Report the malaria status.
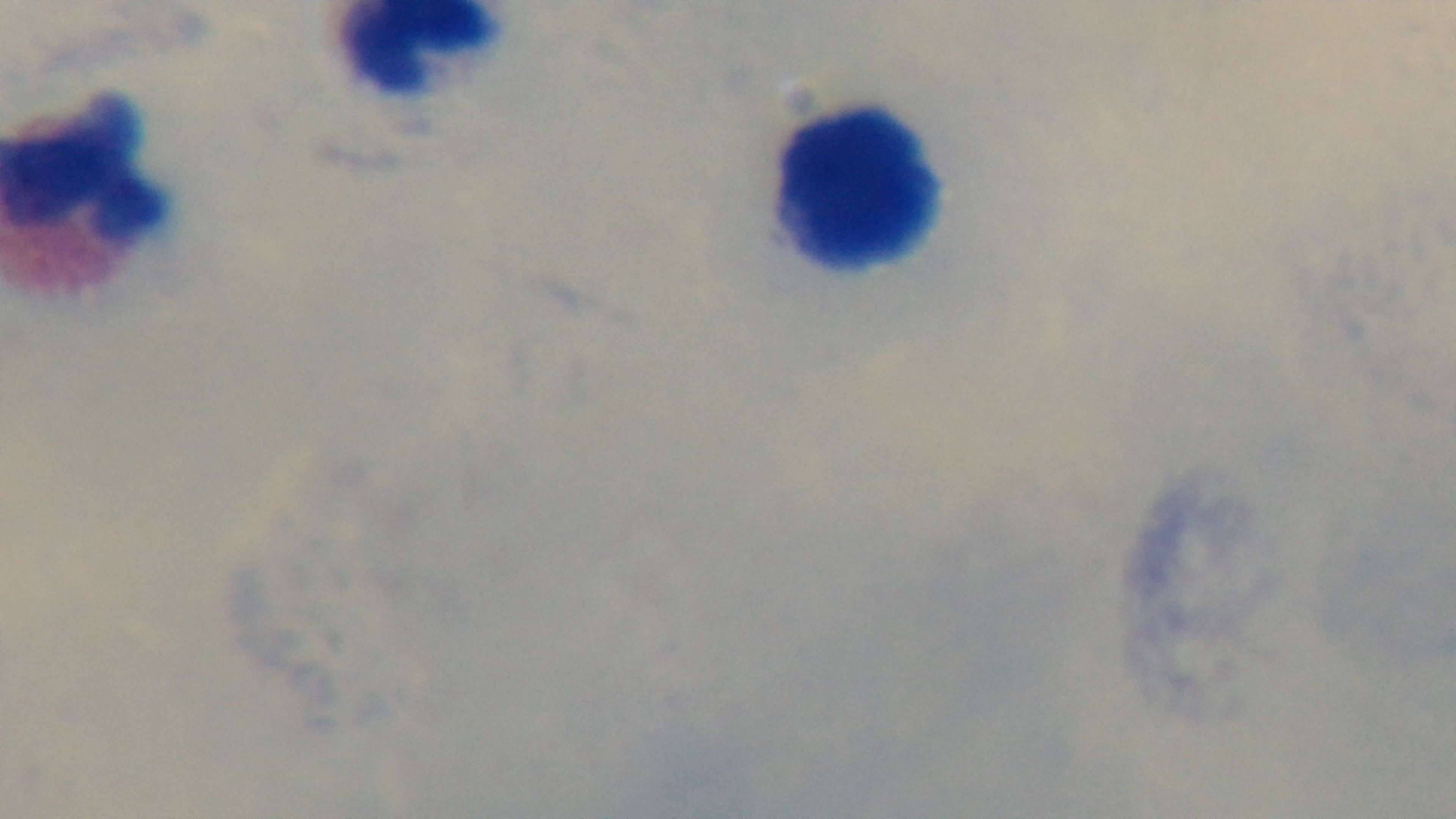

Uninfected.

Summary:
  - Preparation: thick blood film
  - Modality: light microscopy
  - Stain: Giemsa
  - Capture: mounted 4K digital camera
  - Objective: 100x oil immersion
  - Field of view: one from the slide